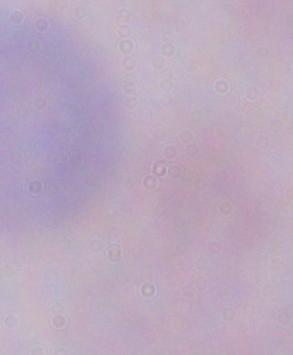

Summary:
  - Magnification: 1000x
  - Modality: photomicrograph
  - Identification: trypanosome